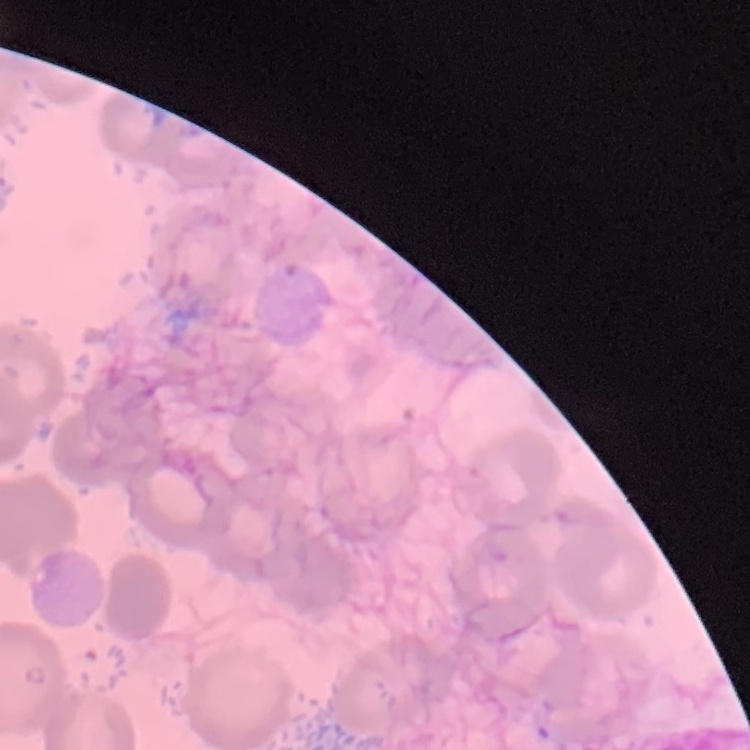
The red blood cells show no rouleaux formation. Square crop of a larger photomicrograph. Thin blood smear. Field's or Giemsa stain.